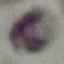 Malaria status: uninfected. Automatically extracted cell patch, resized to 64 × 64 pixels. Thin smear of blood. Giemsa-stained preparation. Photographed with a smartphone camera at the microscope eyepiece.